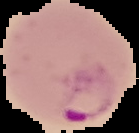
Summary:
  - Image size: 139×133 pixels
  - Image type: segmented cell region on a black background
  - Preparation: thin blood smear
  - Result: malaria parasites identified